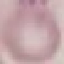
Summary:
  - Malaria status: uninfected
  - Preparation: thin blood film
  - Capture: smartphone camera at the microscope eyepiece
  - Stain: Giemsa
  - Image type: cell patch, automatically extracted from a larger field of view and resized to 64 × 64 pixels